Identify the parasite.
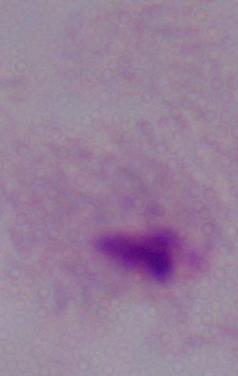

This is a trichomonad.

modality: micrograph
magnification: 1000x